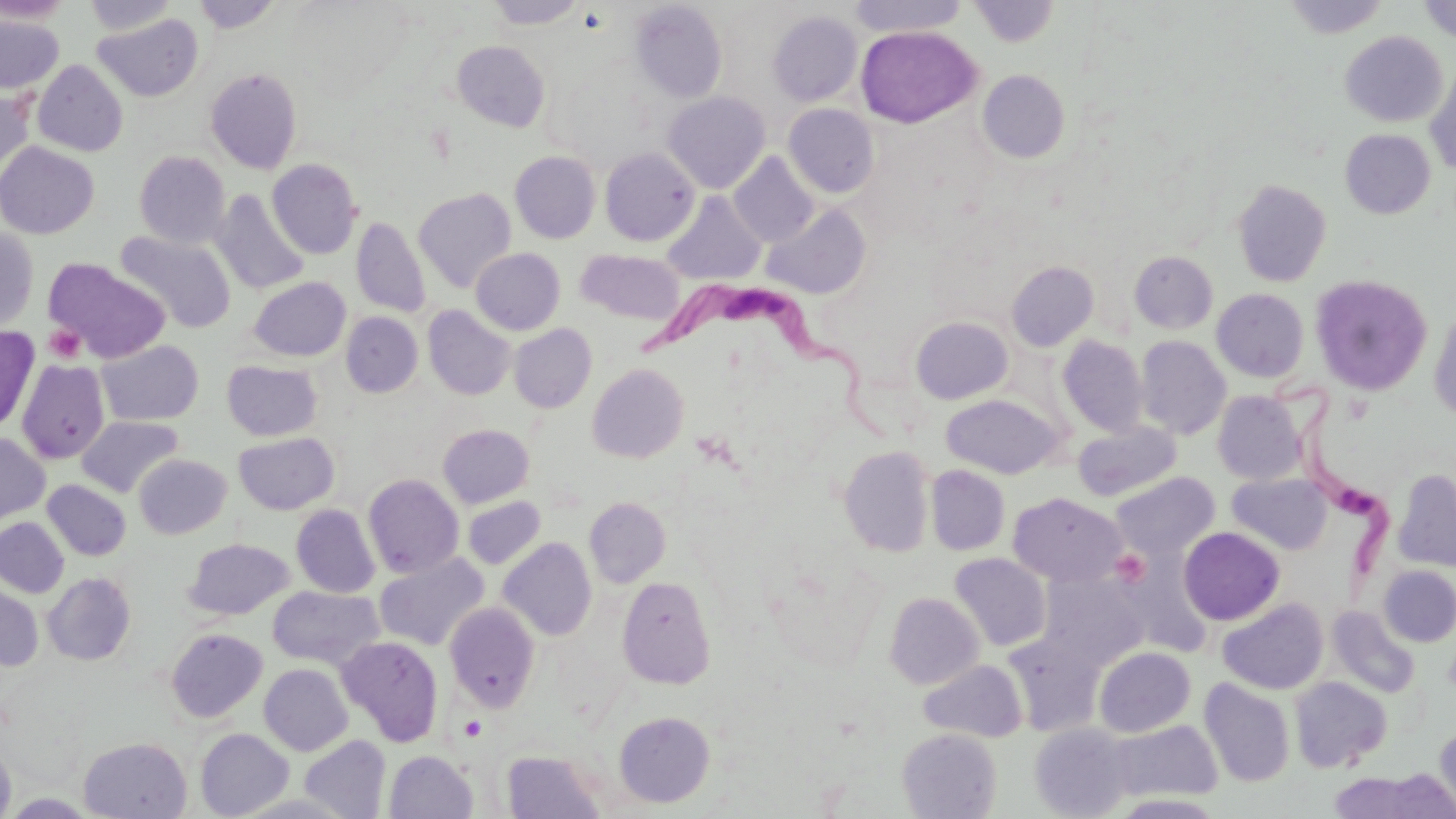 Approximate bounding boxes as named x1/y1/x2/y2 corners in pixels. Trypanosoma brucei locations: (x1=647, y1=285, x2=901, y2=439), (x1=1272, y1=365, x2=1400, y2=592). Uninfected red blood cell locations: (x1=0, y1=0, x2=73, y2=24), (x1=83, y1=0, x2=178, y2=36), (x1=486, y1=0, x2=586, y2=29), (x1=848, y1=0, x2=969, y2=37), (x1=1283, y1=0, x2=1389, y2=39), (x1=1417, y1=0, x2=1456, y2=44), (x1=192, y1=1, x2=283, y2=33), (x1=630, y1=1, x2=728, y2=103), (x1=970, y1=1, x2=1059, y2=47), (x1=767, y1=10, x2=863, y2=106), (x1=776, y1=11, x2=869, y2=198), (x1=93, y1=13, x2=204, y2=102), (x1=0, y1=15, x2=64, y2=94), (x1=855, y1=25, x2=981, y2=128), (x1=1340, y1=31, x2=1448, y2=127), (x1=452, y1=40, x2=550, y2=132), (x1=32, y1=60, x2=128, y2=156), (x1=1425, y1=65, x2=1456, y2=176), (x1=206, y1=67, x2=303, y2=174), (x1=978, y1=69, x2=1070, y2=163), (x1=0, y1=84, x2=35, y2=180), (x1=662, y1=91, x2=771, y2=193), (x1=783, y1=103, x2=879, y2=197), (x1=1340, y1=129, x2=1436, y2=218), (x1=0, y1=141, x2=99, y2=239), (x1=600, y1=146, x2=699, y2=246), (x1=134, y1=150, x2=230, y2=248), (x1=510, y1=151, x2=601, y2=243), (x1=728, y1=153, x2=818, y2=247), (x1=267, y1=158, x2=363, y2=259), (x1=1232, y1=178, x2=1331, y2=288), (x1=413, y1=187, x2=516, y2=292), (x1=212, y1=189, x2=309, y2=296), (x1=662, y1=191, x2=767, y2=285), (x1=762, y1=204, x2=871, y2=299), (x1=351, y1=216, x2=430, y2=318), (x1=0, y1=227, x2=39, y2=333), (x1=115, y1=230, x2=236, y2=333), (x1=471, y1=247, x2=565, y2=335), (x1=576, y1=249, x2=686, y2=326), (x1=1130, y1=251, x2=1218, y2=333), (x1=44, y1=258, x2=171, y2=363), (x1=1007, y1=261, x2=1099, y2=351), (x1=1310, y1=274, x2=1433, y2=396), (x1=249, y1=277, x2=351, y2=361), (x1=1212, y1=288, x2=1308, y2=382), (x1=1429, y1=304, x2=1456, y2=423), (x1=422, y1=306, x2=515, y2=400), (x1=341, y1=312, x2=423, y2=397), (x1=910, y1=316, x2=1013, y2=405), (x1=509, y1=323, x2=596, y2=413), (x1=0, y1=326, x2=39, y2=433), (x1=1057, y1=336, x2=1148, y2=437), (x1=1136, y1=336, x2=1231, y2=439), (x1=96, y1=339, x2=204, y2=426), (x1=17, y1=359, x2=109, y2=464), (x1=222, y1=360, x2=323, y2=441), (x1=587, y1=363, x2=690, y2=462), (x1=1212, y1=391, x2=1305, y2=485), (x1=940, y1=394, x2=1066, y2=478), (x1=77, y1=415, x2=184, y2=497), (x1=1072, y1=420, x2=1182, y2=502), (x1=437, y1=423, x2=534, y2=508), (x1=233, y1=431, x2=339, y2=515), (x1=0, y1=432, x2=49, y2=524), (x1=840, y1=446, x2=935, y2=557), (x1=133, y1=454, x2=231, y2=539), (x1=926, y1=465, x2=1010, y2=555), (x1=1393, y1=468, x2=1456, y2=572), (x1=1111, y1=472, x2=1219, y2=559), (x1=1227, y1=473, x2=1332, y2=555), (x1=363, y1=474, x2=464, y2=579), (x1=42, y1=479, x2=131, y2=561), (x1=1008, y1=492, x2=1127, y2=587), (x1=463, y1=496, x2=546, y2=569), (x1=584, y1=497, x2=672, y2=587), (x1=291, y1=504, x2=380, y2=597), (x1=0, y1=517, x2=69, y2=598), (x1=1178, y1=527, x2=1285, y2=625), (x1=499, y1=537, x2=597, y2=640), (x1=184, y1=538, x2=294, y2=620), (x1=374, y1=553, x2=489, y2=651), (x1=949, y1=553, x2=1052, y2=651), (x1=1378, y1=565, x2=1456, y2=647), (x1=43, y1=572, x2=136, y2=665), (x1=1039, y1=573, x2=1149, y2=669), (x1=617, y1=575, x2=717, y2=688), (x1=0, y1=584, x2=43, y2=671), (x1=268, y1=585, x2=383, y2=669), (x1=884, y1=592, x2=984, y2=689), (x1=1217, y1=598, x2=1328, y2=694), (x1=444, y1=602, x2=540, y2=712), (x1=1327, y1=605, x2=1420, y2=697), (x1=166, y1=628, x2=268, y2=722), (x1=337, y1=635, x2=444, y2=747), (x1=1003, y1=635, x2=1103, y2=736), (x1=1093, y1=647, x2=1196, y2=737), (x1=919, y1=659, x2=1027, y2=742), (x1=259, y1=663, x2=353, y2=756), (x1=1289, y1=676, x2=1391, y2=772), (x1=1199, y1=678, x2=1295, y2=786), (x1=614, y1=712, x2=715, y2=808), (x1=1108, y1=719, x2=1223, y2=803), (x1=1028, y1=722, x2=1133, y2=818), (x1=1435, y1=722, x2=1456, y2=814), (x1=196, y1=728, x2=294, y2=818), (x1=897, y1=728, x2=1002, y2=818), (x1=299, y1=735, x2=391, y2=819), (x1=78, y1=737, x2=192, y2=818), (x1=0, y1=741, x2=16, y2=819), (x1=501, y1=749, x2=606, y2=818), (x1=385, y1=750, x2=478, y2=818), (x1=1327, y1=773, x2=1435, y2=818). Platelet locations: (x1=44, y1=324, x2=86, y2=364), (x1=1111, y1=549, x2=1151, y2=587). Slide-level diagnosis: Trypanosoma brucei. Optical microscopy. Image is 1456×819 pixels. One field of a larger specimen. Thin blood smear. 1000x magnification. May-Grünwald-Giemsa stain.